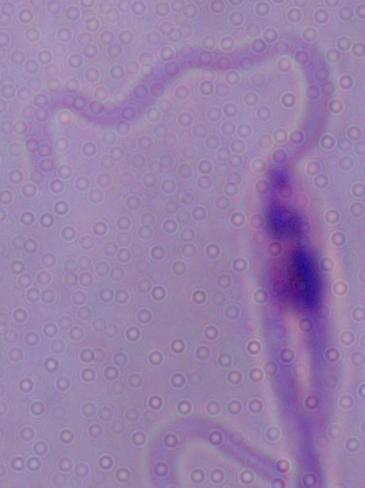
Summary:
  - Magnification: 1000x
  - Identification: Leishmania
  - Modality: photomicrograph